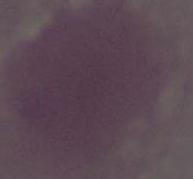

identification: erythrocyte
magnification: 1000x
modality: micrograph